Assess the morphology of the red blood cells.
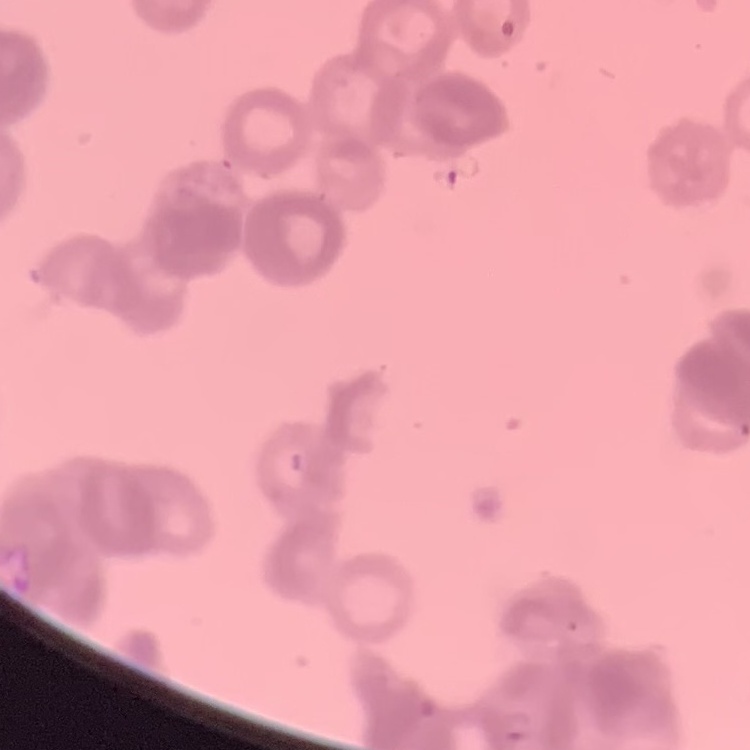
They show rouleaux formation.

Field's or Giemsa stain. Square crop of a larger photomicrograph. Thin blood film.